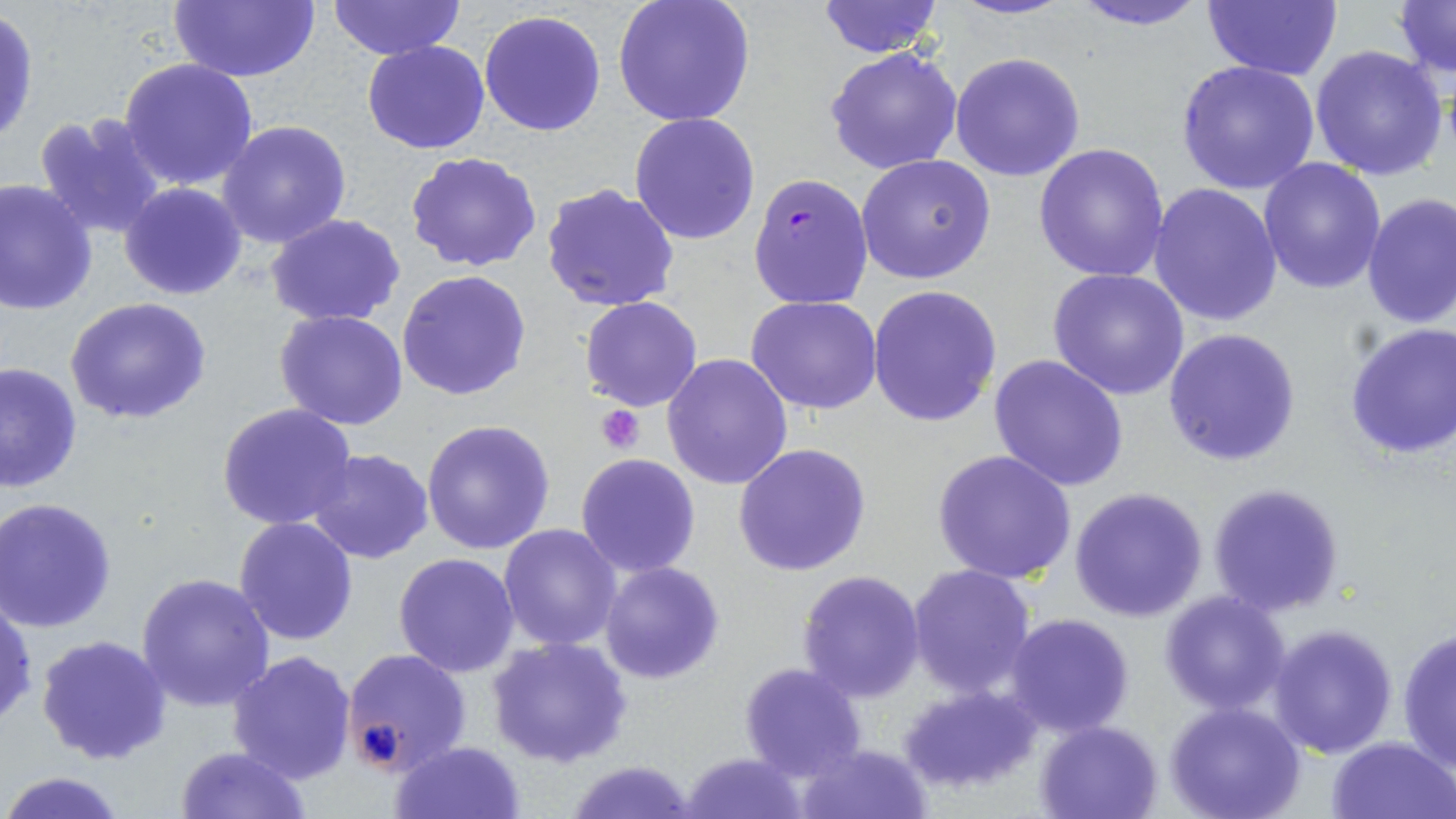

Approximate bounding boxes as (x1, y1, x2, y2) in pixels. Platelet locations: (597, 405, 646, 453). Plasmodium falciparum-infected red blood cell locations: (746, 173, 873, 309). Uninfected red blood cell locations: (167, 0, 322, 85), (611, 0, 755, 126), (816, 0, 945, 58), (950, 0, 1075, 22), (1065, 0, 1213, 30), (326, 1, 464, 61), (1200, 1, 1342, 81), (1392, 1, 1454, 78), (478, 9, 607, 138), (1, 10, 38, 147), (362, 40, 491, 154), (1308, 44, 1450, 181), (826, 47, 963, 175), (949, 52, 1085, 181), (118, 57, 261, 191), (1176, 59, 1320, 195), (33, 111, 168, 242), (630, 113, 762, 245), (217, 119, 352, 250), (1033, 144, 1171, 284), (405, 151, 542, 272), (856, 154, 996, 286), (1258, 157, 1387, 294), (0, 179, 98, 315), (119, 181, 247, 301), (1147, 182, 1283, 328), (538, 183, 682, 315), (1360, 194, 1456, 328), (265, 213, 407, 327), (1047, 267, 1190, 400), (397, 269, 531, 401), (869, 285, 1002, 426), (580, 296, 703, 412), (747, 296, 883, 415), (65, 297, 212, 425), (275, 309, 408, 430), (1343, 320, 1456, 460), (1163, 328, 1300, 467), (661, 352, 793, 489), (987, 354, 1130, 492), (0, 360, 82, 493), (217, 404, 359, 531), (421, 419, 554, 556), (734, 444, 874, 578), (932, 449, 1077, 585), (307, 450, 435, 565), (575, 455, 702, 578), (1207, 483, 1345, 617), (1067, 487, 1210, 623), (2, 498, 119, 632), (233, 517, 359, 645), (497, 522, 623, 651), (394, 552, 521, 677), (599, 562, 726, 683), (906, 564, 1037, 699), (796, 569, 926, 703), (136, 571, 275, 710), (1158, 590, 1293, 714), (0, 595, 36, 729), (1005, 613, 1134, 738), (1269, 623, 1398, 758), (1396, 625, 1456, 773), (35, 632, 171, 765), (485, 636, 632, 768), (340, 647, 473, 776), (226, 649, 359, 784), (739, 661, 867, 781), (900, 683, 1038, 797), (1165, 702, 1306, 819), (1034, 719, 1165, 818), (1326, 736, 1454, 819), (389, 740, 527, 819), (794, 742, 934, 819), (175, 744, 312, 818), (682, 751, 807, 819), (564, 757, 702, 819), (1, 770, 131, 819). Slide-level diagnosis: Plasmodium falciparum. Optical microscopy. May-Grünwald-Giemsa stain. Thin blood film. Image is 1456×819 pixels. One field of a larger specimen. 1000x magnification.